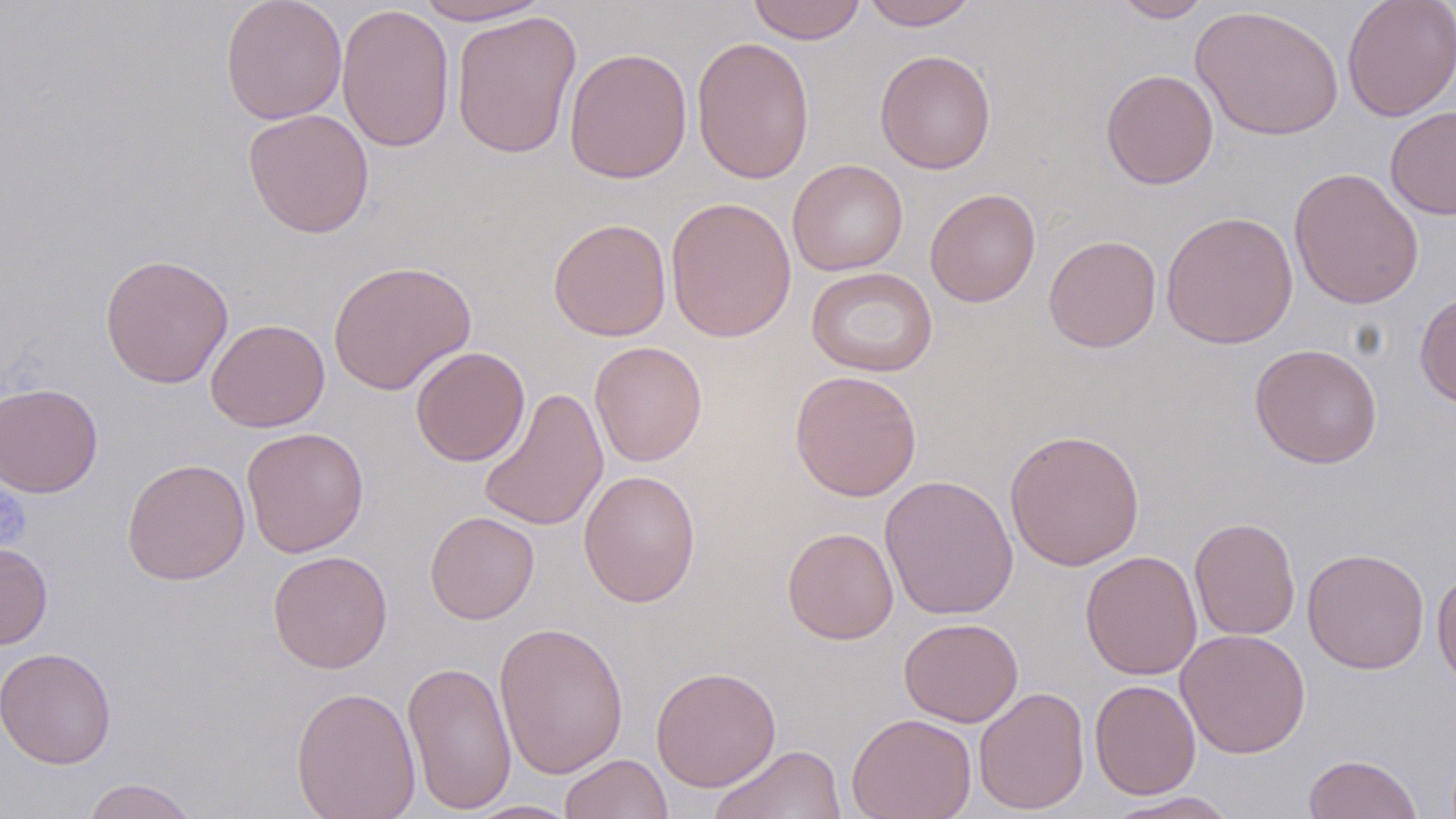

slide-level diagnosis = negative for blood parasites
modality = light microscopy
magnification = 1000x
uninfected red blood cell locations = approximate bounding boxes as named x1/y1/x2/y2 corners in pixels: (x1=220, y1=0, x2=347, y2=125), (x1=412, y1=0, x2=551, y2=25), (x1=747, y1=0, x2=867, y2=44), (x1=861, y1=0, x2=979, y2=30), (x1=1112, y1=0, x2=1213, y2=22), (x1=1342, y1=0, x2=1456, y2=121), (x1=336, y1=3, x2=455, y2=153), (x1=1191, y1=4, x2=1344, y2=141), (x1=451, y1=10, x2=582, y2=160), (x1=691, y1=36, x2=815, y2=185), (x1=564, y1=46, x2=693, y2=184), (x1=875, y1=49, x2=996, y2=174), (x1=1100, y1=69, x2=1219, y2=189), (x1=1385, y1=105, x2=1456, y2=220), (x1=242, y1=107, x2=375, y2=238), (x1=787, y1=159, x2=908, y2=277), (x1=1288, y1=166, x2=1424, y2=311), (x1=924, y1=187, x2=1041, y2=307), (x1=665, y1=196, x2=797, y2=343), (x1=1160, y1=211, x2=1299, y2=349), (x1=548, y1=218, x2=672, y2=341), (x1=1043, y1=234, x2=1162, y2=352), (x1=99, y1=253, x2=234, y2=389), (x1=328, y1=260, x2=476, y2=396), (x1=806, y1=267, x2=938, y2=378), (x1=1414, y1=291, x2=1456, y2=409), (x1=205, y1=318, x2=330, y2=433), (x1=590, y1=341, x2=707, y2=467), (x1=1249, y1=343, x2=1383, y2=468), (x1=410, y1=346, x2=530, y2=467), (x1=789, y1=369, x2=922, y2=501), (x1=0, y1=382, x2=103, y2=498), (x1=477, y1=386, x2=609, y2=532), (x1=241, y1=426, x2=369, y2=558), (x1=1004, y1=429, x2=1145, y2=571), (x1=122, y1=458, x2=250, y2=585), (x1=578, y1=469, x2=701, y2=608), (x1=879, y1=474, x2=1019, y2=621), (x1=425, y1=511, x2=539, y2=624), (x1=1189, y1=517, x2=1302, y2=640), (x1=782, y1=527, x2=899, y2=645), (x1=0, y1=542, x2=53, y2=649), (x1=1302, y1=547, x2=1430, y2=674), (x1=267, y1=550, x2=393, y2=673), (x1=1080, y1=550, x2=1203, y2=680), (x1=1432, y1=570, x2=1456, y2=691), (x1=898, y1=617, x2=1023, y2=727), (x1=494, y1=620, x2=629, y2=779), (x1=1175, y1=628, x2=1311, y2=759), (x1=1, y1=647, x2=117, y2=769), (x1=402, y1=660, x2=518, y2=815), (x1=651, y1=665, x2=782, y2=792), (x1=1089, y1=679, x2=1201, y2=799), (x1=290, y1=685, x2=421, y2=819), (x1=974, y1=686, x2=1090, y2=815), (x1=846, y1=712, x2=977, y2=819), (x1=709, y1=744, x2=847, y2=819), (x1=560, y1=753, x2=673, y2=819), (x1=1304, y1=753, x2=1423, y2=819), (x1=80, y1=778, x2=200, y2=819), (x1=1103, y1=791, x2=1242, y2=818), (x1=461, y1=799, x2=581, y2=818)
stain = May-Grünwald-Giemsa
image size = 1456×819 pixels
field of view = single
preparation = thin blood smear
platelet locations = approximate bounding boxes as named x1/y1/x2/y2 corners in pixels: (x1=0, y1=487, x2=31, y2=548)